Assess for malaria.
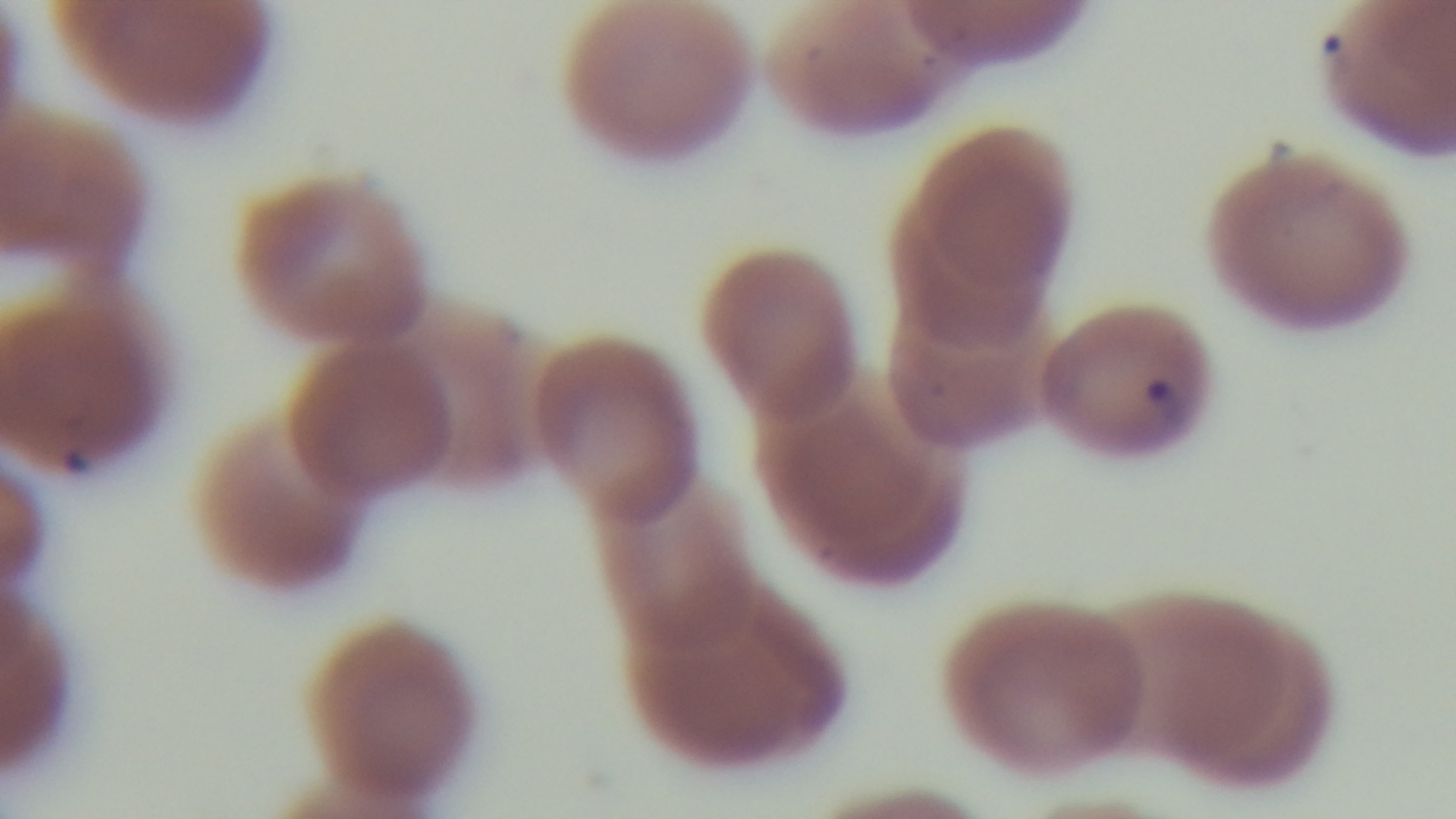

It is infected.

preparation: thin smear
field_of_view: single
modality: light microscopy
objective: 100x oil immersion
capture: mounted 4K digital camera
stain: Giemsa